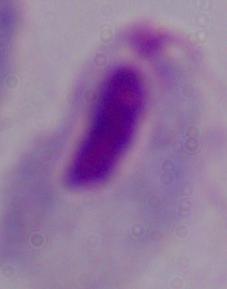
magnification = 1000x
identification = trichomonad
modality = micrograph